Classify this cell by malaria status.
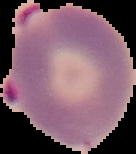
It is parasitized.

Summary:
  - Image size: 136×154 pixels
  - Preparation: thin blood smear
  - Image type: segmented cell region with the area outside set to black